Identify the parasite.
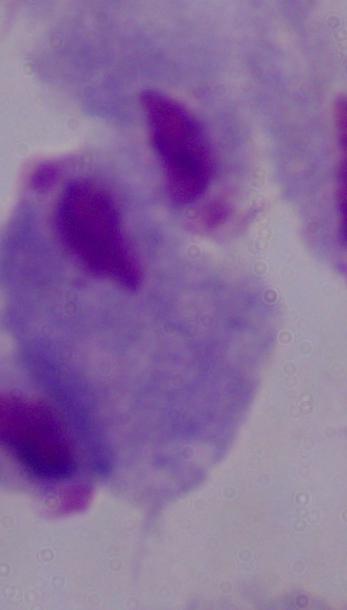
A trichomonad.

Summary:
  - Modality: photomicrograph
  - Magnification: 1000x